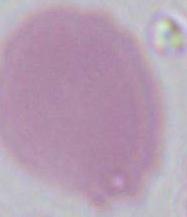

{
  "magnification": "1000x",
  "modality": "photomicrograph",
  "identification": "red blood cell"
}